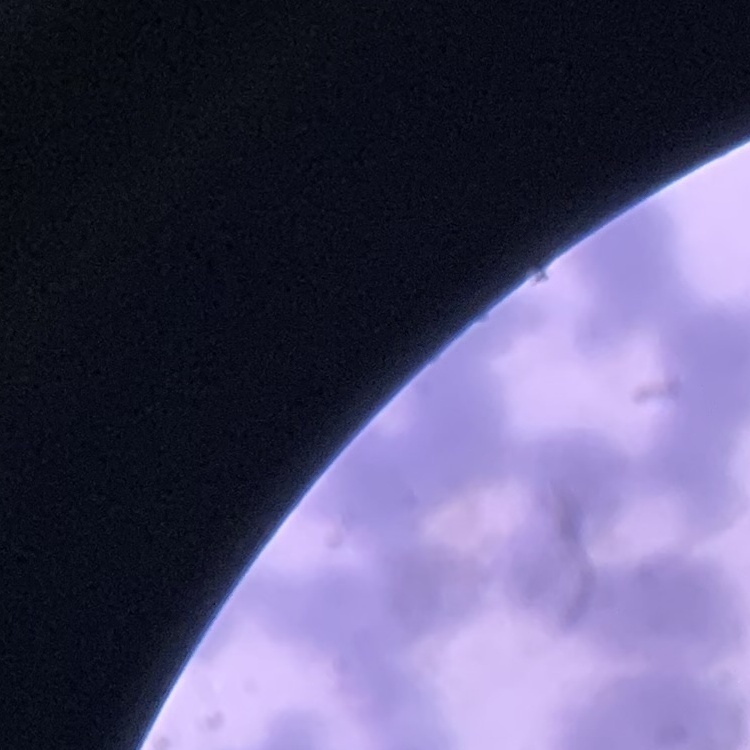

erythrocyte morphology = rouleaux formation
preparation = thin blood film
image type = square crop of a larger photomicrograph
stain = Field's or Giemsa